Report the malaria status of this cell.
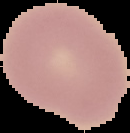

It is uninfected.

Cell region segmented out of the field of view; the surrounding area is masked to black. Image is 130×133 pixels. From a thin blood smear.